Assess this cell for malaria.
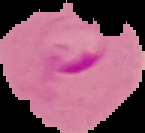
It is parasitized.

Cell region segmented out of the field of view; the surrounding area is masked to black. Image is 145×133 pixels. From a thin blood film.